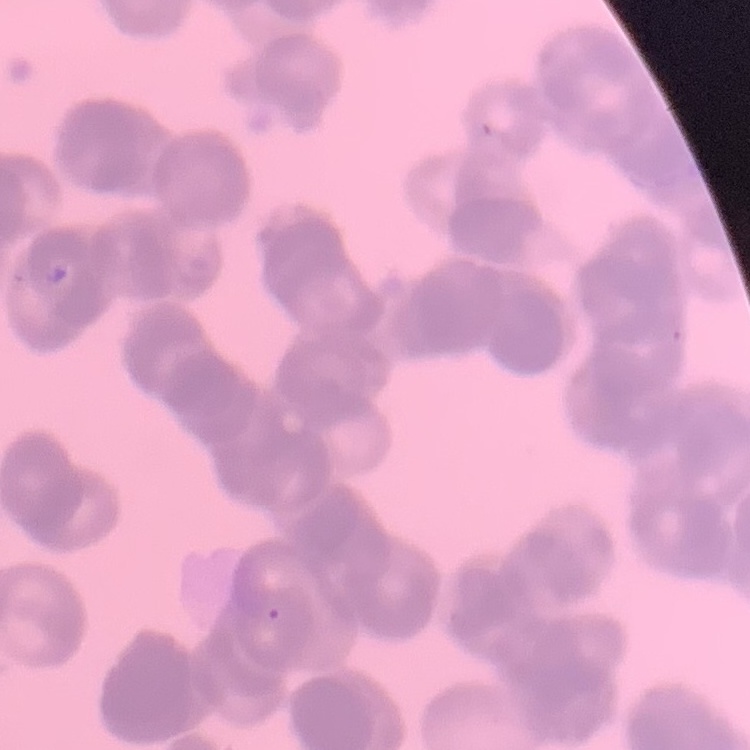
The red blood cells show rouleaux formation. Thin blood smear. Stained with either Field's or Giemsa. Square crop of a larger photomicrograph.